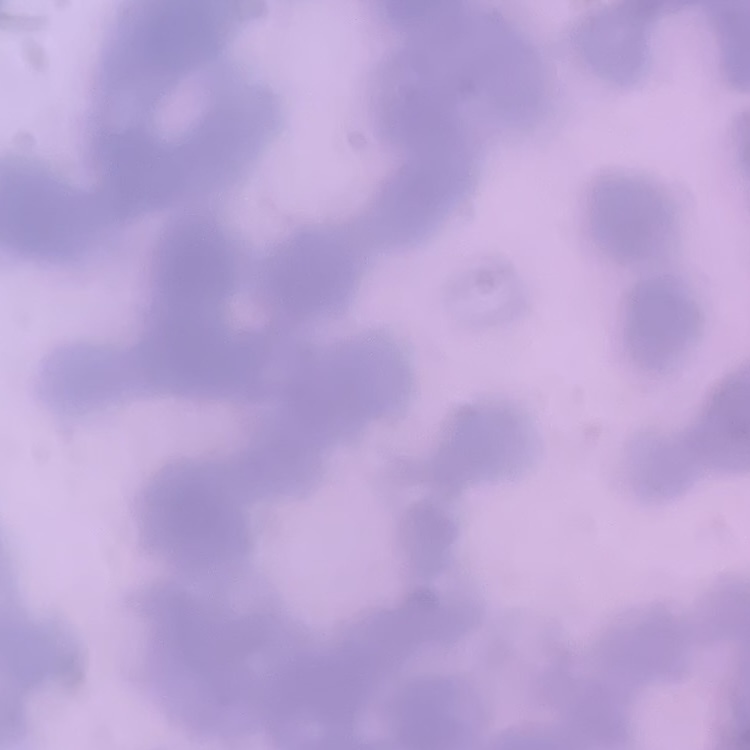
erythrocyte_morphology: rouleaux formation
preparation: thin blood film
stain: Field's or Giemsa
image_type: one tile cut from a larger photomicrograph